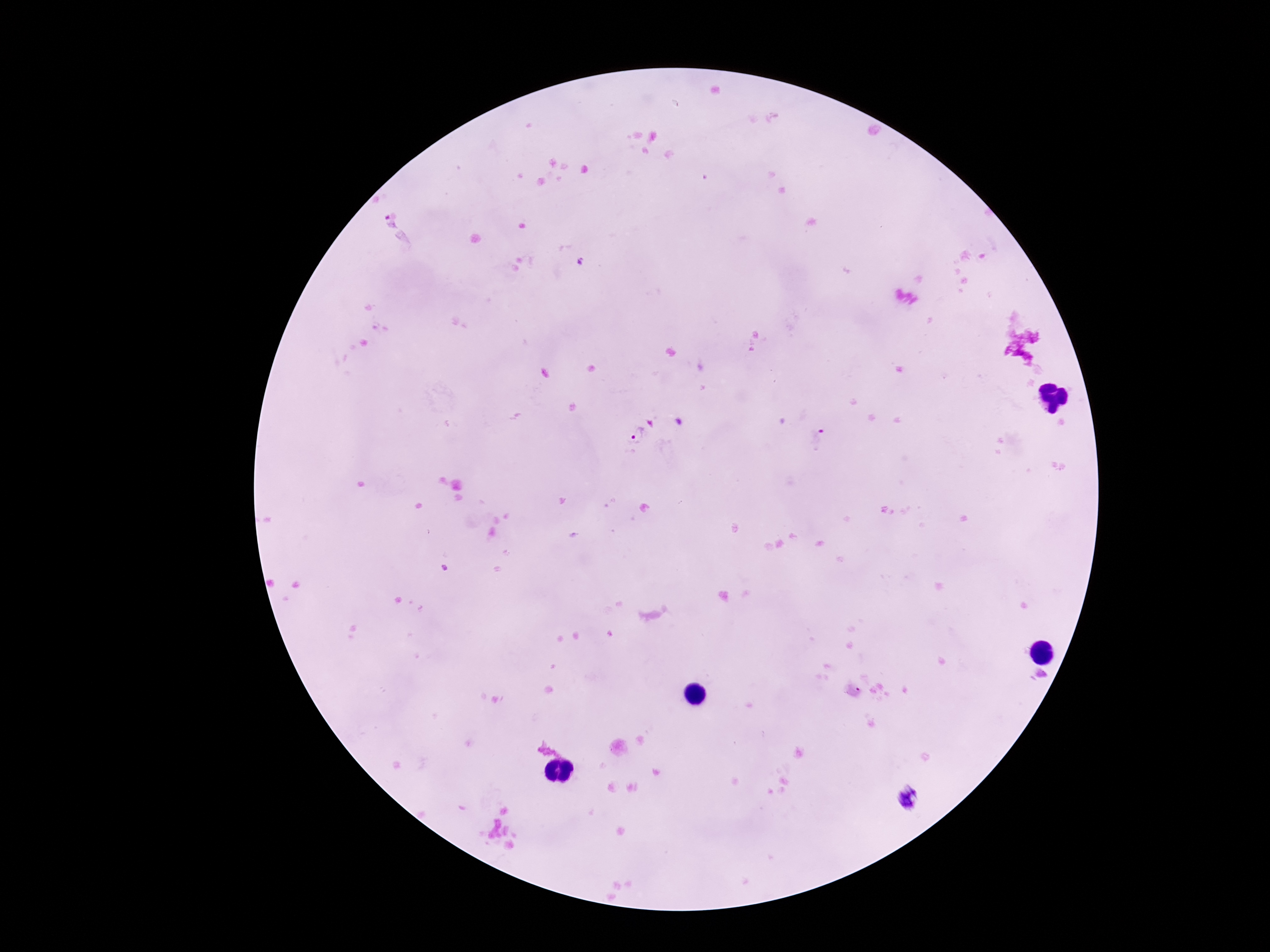

Approximate object centers, in pixels from the top-left corner.
Summary:
  - Plasmodium parasite locations: (x=387, y=224), (x=638, y=435), (x=818, y=439), (x=911, y=799)
  - Stain: Giemsa
  - Image size: 1270×952 pixels
  - Patient malaria status: infected
  - Field of view: one from this slide
  - Preparation: thick blood smear
  - Capture: smartphone camera through the microscope eyepiece
  - Magnification: 100x